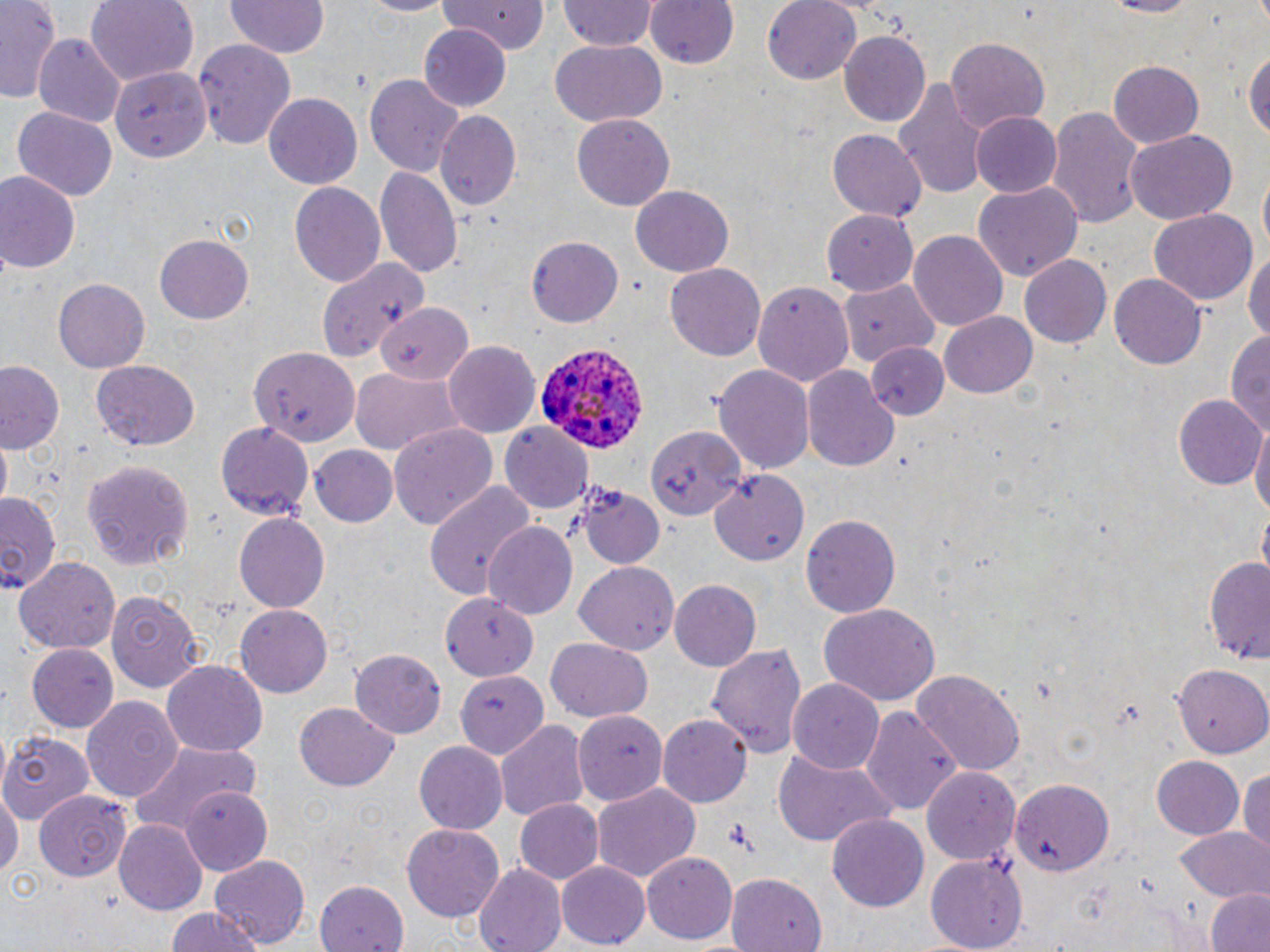
Plasmodium ovale-infected red blood cell locations = approximate bounding boxes as named x1/y1/x2/y2 corners in pixels: (x1=532, y1=338, x2=650, y2=455)
slide-level diagnosis = Plasmodium ovale
image size = 1270×952 pixels
preparation = thin blood smear
modality = optical microscopy
field of view = one of a larger specimen
uninfected red blood cell locations = approximate bounding boxes as named x1/y1/x2/y2 corners in pixels: (x1=0, y1=0, x2=62, y2=105), (x1=85, y1=0, x2=197, y2=84), (x1=354, y1=0, x2=458, y2=16), (x1=439, y1=0, x2=552, y2=55), (x1=645, y1=0, x2=737, y2=71), (x1=763, y1=0, x2=862, y2=84), (x1=1096, y1=0, x2=1203, y2=18), (x1=225, y1=1, x2=329, y2=61), (x1=557, y1=1, x2=658, y2=52), (x1=419, y1=27, x2=512, y2=110), (x1=838, y1=29, x2=931, y2=129), (x1=32, y1=36, x2=124, y2=126), (x1=946, y1=36, x2=1049, y2=135), (x1=193, y1=37, x2=296, y2=147), (x1=549, y1=40, x2=667, y2=126), (x1=1244, y1=43, x2=1269, y2=148), (x1=1108, y1=61, x2=1202, y2=149), (x1=111, y1=64, x2=214, y2=161), (x1=365, y1=74, x2=467, y2=179), (x1=895, y1=78, x2=988, y2=197), (x1=264, y1=94, x2=362, y2=191), (x1=9, y1=106, x2=118, y2=203), (x1=1047, y1=106, x2=1145, y2=226), (x1=433, y1=110, x2=523, y2=211), (x1=970, y1=112, x2=1061, y2=197), (x1=572, y1=114, x2=675, y2=211), (x1=1125, y1=129, x2=1237, y2=225), (x1=827, y1=130, x2=929, y2=224), (x1=377, y1=164, x2=463, y2=277), (x1=0, y1=170, x2=81, y2=274), (x1=290, y1=181, x2=387, y2=290), (x1=974, y1=182, x2=1080, y2=283), (x1=631, y1=184, x2=734, y2=277), (x1=823, y1=208, x2=917, y2=296), (x1=1150, y1=209, x2=1257, y2=305), (x1=910, y1=231, x2=1007, y2=333), (x1=154, y1=234, x2=254, y2=324), (x1=526, y1=236, x2=623, y2=328), (x1=1244, y1=245, x2=1270, y2=353), (x1=1020, y1=255, x2=1111, y2=346), (x1=312, y1=256, x2=429, y2=367), (x1=665, y1=263, x2=767, y2=360), (x1=1110, y1=272, x2=1207, y2=369), (x1=54, y1=278, x2=151, y2=371), (x1=752, y1=278, x2=854, y2=384), (x1=842, y1=279, x2=941, y2=367), (x1=376, y1=303, x2=472, y2=385), (x1=940, y1=311, x2=1039, y2=399), (x1=1224, y1=329, x2=1270, y2=441), (x1=444, y1=339, x2=542, y2=438), (x1=867, y1=343, x2=950, y2=420), (x1=249, y1=350, x2=362, y2=446), (x1=0, y1=360, x2=64, y2=455), (x1=92, y1=361, x2=203, y2=451), (x1=713, y1=363, x2=817, y2=473), (x1=802, y1=365, x2=899, y2=472), (x1=351, y1=368, x2=464, y2=456), (x1=1175, y1=394, x2=1265, y2=490), (x1=1251, y1=418, x2=1270, y2=528), (x1=219, y1=420, x2=310, y2=519), (x1=501, y1=422, x2=592, y2=512), (x1=646, y1=424, x2=744, y2=524), (x1=389, y1=425, x2=496, y2=531), (x1=310, y1=446, x2=399, y2=528), (x1=84, y1=457, x2=193, y2=573), (x1=709, y1=471, x2=811, y2=566), (x1=424, y1=480, x2=533, y2=603), (x1=572, y1=483, x2=665, y2=572), (x1=0, y1=493, x2=60, y2=593), (x1=233, y1=513, x2=329, y2=612), (x1=802, y1=514, x2=901, y2=619), (x1=484, y1=520, x2=578, y2=617), (x1=16, y1=555, x2=119, y2=654), (x1=1206, y1=556, x2=1270, y2=663), (x1=574, y1=561, x2=679, y2=656), (x1=672, y1=579, x2=762, y2=672), (x1=107, y1=590, x2=202, y2=694), (x1=439, y1=590, x2=541, y2=680), (x1=818, y1=603, x2=939, y2=704), (x1=235, y1=605, x2=334, y2=697), (x1=545, y1=639, x2=651, y2=721), (x1=708, y1=641, x2=807, y2=756), (x1=27, y1=643, x2=117, y2=733), (x1=350, y1=649, x2=449, y2=737), (x1=162, y1=661, x2=268, y2=760), (x1=1172, y1=661, x2=1270, y2=756), (x1=453, y1=670, x2=547, y2=757), (x1=912, y1=670, x2=1025, y2=773), (x1=789, y1=680, x2=883, y2=774), (x1=81, y1=695, x2=182, y2=802), (x1=295, y1=703, x2=398, y2=789), (x1=863, y1=704, x2=963, y2=820), (x1=572, y1=711, x2=670, y2=803), (x1=660, y1=714, x2=752, y2=807), (x1=495, y1=718, x2=588, y2=820), (x1=0, y1=728, x2=95, y2=822), (x1=130, y1=737, x2=259, y2=838), (x1=415, y1=741, x2=509, y2=834), (x1=771, y1=748, x2=898, y2=847), (x1=1152, y1=755, x2=1245, y2=840), (x1=1239, y1=765, x2=1270, y2=855), (x1=924, y1=767, x2=1021, y2=865), (x1=1008, y1=776, x2=1114, y2=874), (x1=0, y1=783, x2=20, y2=891), (x1=592, y1=783, x2=699, y2=882), (x1=181, y1=786, x2=274, y2=873), (x1=34, y1=794, x2=134, y2=879), (x1=515, y1=798, x2=603, y2=886), (x1=828, y1=814, x2=929, y2=910), (x1=115, y1=820, x2=208, y2=916), (x1=402, y1=821, x2=504, y2=920), (x1=1176, y1=826, x2=1269, y2=901), (x1=642, y1=852, x2=738, y2=944), (x1=925, y1=853, x2=1028, y2=952), (x1=211, y1=856, x2=309, y2=949), (x1=557, y1=862, x2=650, y2=947), (x1=473, y1=863, x2=566, y2=952), (x1=725, y1=871, x2=824, y2=950), (x1=314, y1=877, x2=409, y2=951), (x1=1205, y1=888, x2=1270, y2=952), (x1=160, y1=908, x2=267, y2=952)
stain = May-Grünwald-Giemsa
magnification = 1000x